Assess the morphology of the red blood cells.
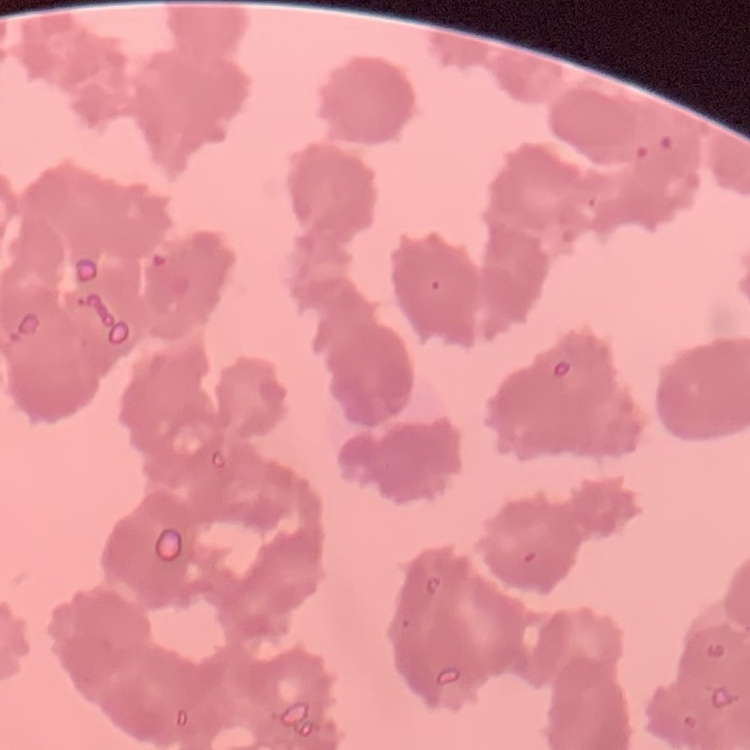

They show rouleaux formation.

image type = square crop of a larger photomicrograph
stain = Field's or Giemsa
preparation = thin peripheral smear